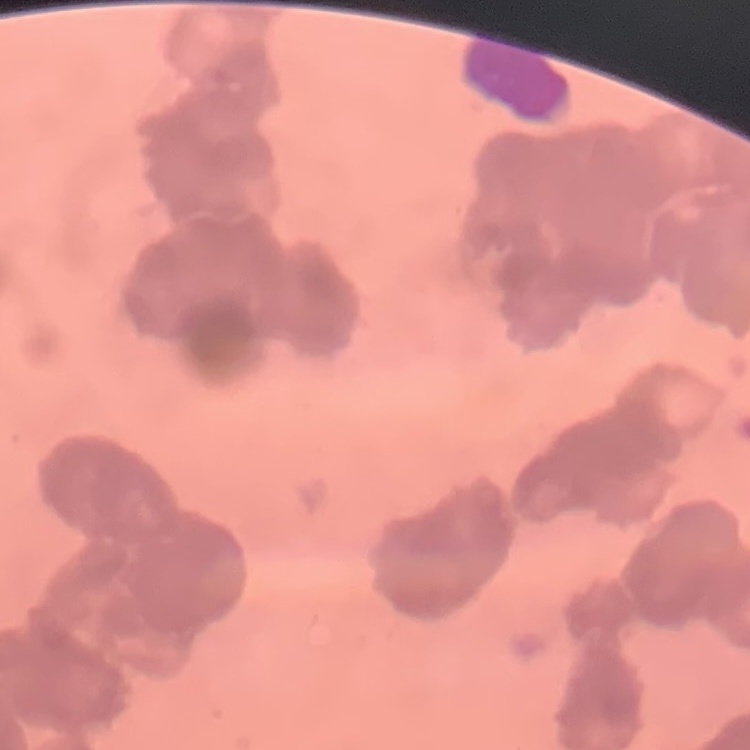
Summary:
  - Erythrocyte morphology: rouleaux formation
  - Image type: one tile cut from a larger photomicrograph
  - Preparation: thin blood smear
  - Stain: Field's or Giemsa